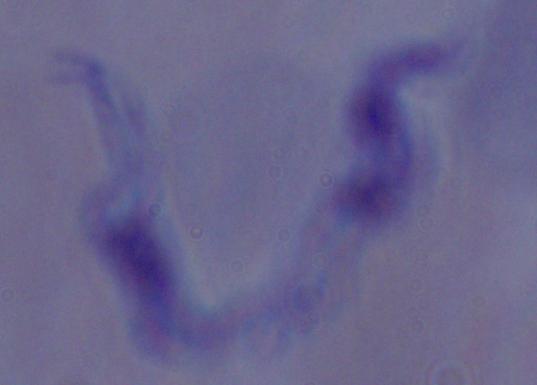

modality = photomicrograph
identification = trypanosome
magnification = 1000x